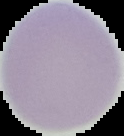
Summary:
  - Malaria status: uninfected
  - Image type: cell region segmented out of the field of view; surrounding area masked to black
  - Preparation: thin blood film
  - Image size: 124×136 pixels